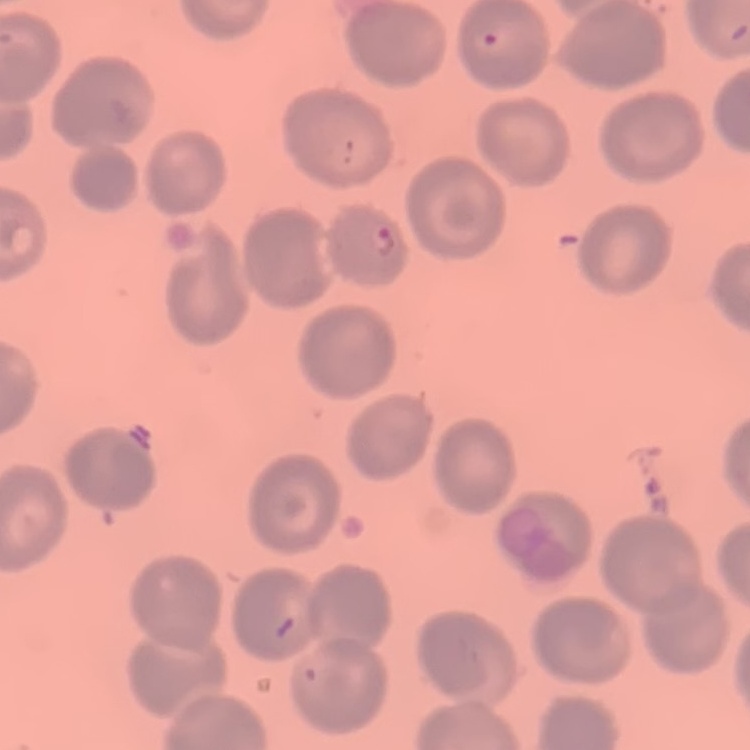

red blood cell morphology = no rouleaux formation
stain = Field's or Giemsa
image type = square crop of a larger photomicrograph
preparation = thin blood smear